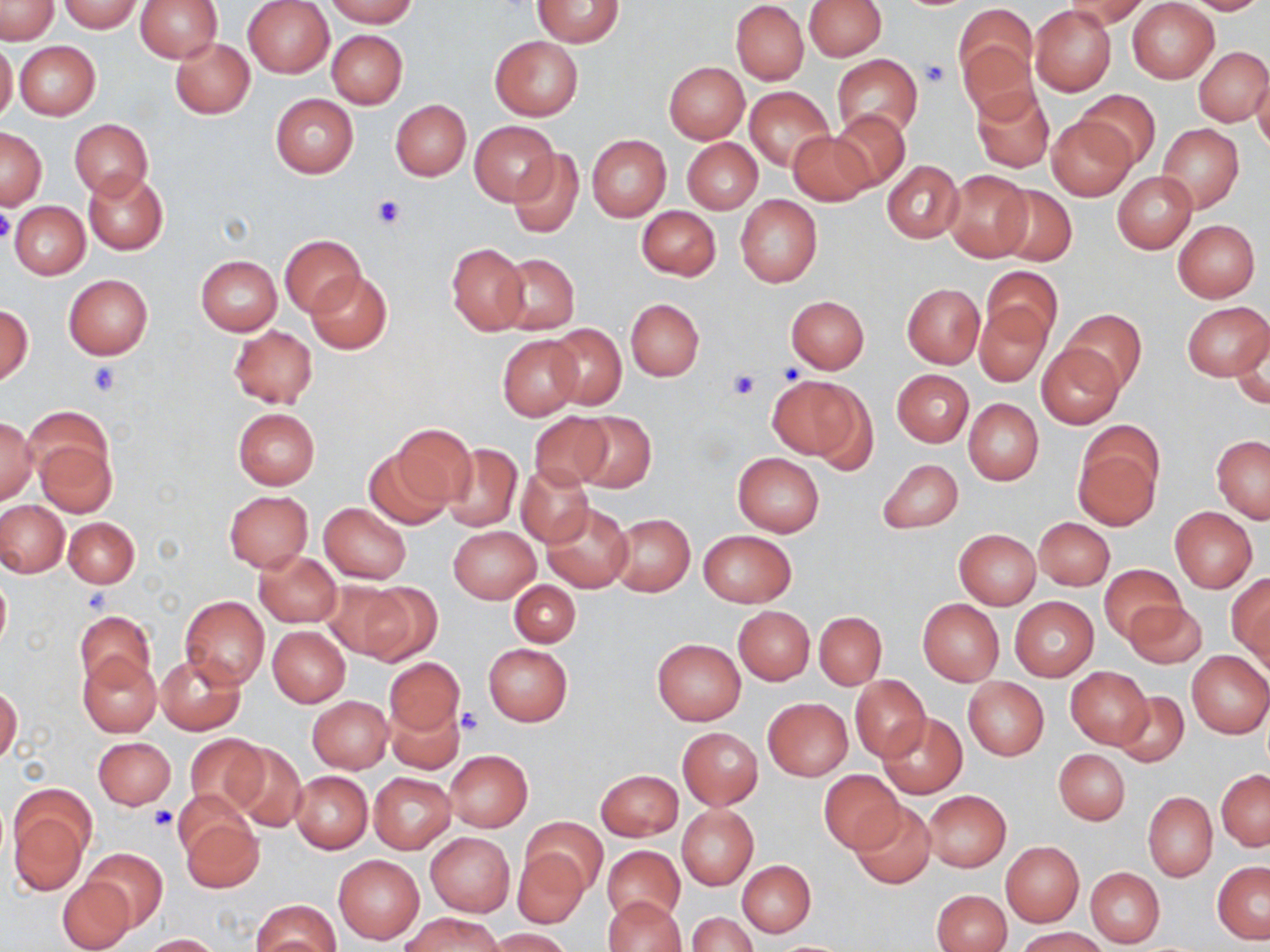 Approximate bounding boxes as named x1/y1/x2/y2 corners in pixels. Uninfected red blood cell locations: (x1=134, y1=0, x2=222, y2=62), (x1=243, y1=0, x2=333, y2=77), (x1=324, y1=0, x2=420, y2=27), (x1=533, y1=0, x2=625, y2=47), (x1=802, y1=0, x2=886, y2=60), (x1=1181, y1=0, x2=1270, y2=15), (x1=0, y1=1, x2=59, y2=43), (x1=61, y1=1, x2=143, y2=32), (x1=731, y1=1, x2=809, y2=84), (x1=1062, y1=1, x2=1147, y2=30), (x1=1127, y1=1, x2=1218, y2=84), (x1=955, y1=4, x2=1036, y2=96), (x1=1030, y1=5, x2=1116, y2=96), (x1=326, y1=29, x2=408, y2=108), (x1=491, y1=36, x2=582, y2=120), (x1=169, y1=37, x2=254, y2=120), (x1=958, y1=39, x2=1040, y2=125), (x1=0, y1=40, x2=18, y2=124), (x1=14, y1=41, x2=100, y2=120), (x1=1195, y1=46, x2=1269, y2=126), (x1=832, y1=54, x2=923, y2=138), (x1=663, y1=61, x2=749, y2=143), (x1=1251, y1=72, x2=1270, y2=153), (x1=972, y1=85, x2=1053, y2=171), (x1=745, y1=86, x2=834, y2=172), (x1=1075, y1=90, x2=1160, y2=172), (x1=271, y1=94, x2=358, y2=178), (x1=391, y1=99, x2=471, y2=181), (x1=830, y1=110, x2=910, y2=191), (x1=1047, y1=115, x2=1135, y2=200), (x1=70, y1=119, x2=152, y2=198), (x1=470, y1=121, x2=556, y2=203), (x1=1157, y1=124, x2=1244, y2=212), (x1=0, y1=128, x2=46, y2=208), (x1=787, y1=131, x2=872, y2=204), (x1=587, y1=135, x2=670, y2=220), (x1=682, y1=138, x2=761, y2=214), (x1=508, y1=147, x2=582, y2=239), (x1=883, y1=161, x2=963, y2=242), (x1=942, y1=169, x2=1033, y2=261), (x1=83, y1=171, x2=168, y2=255), (x1=1113, y1=171, x2=1196, y2=253), (x1=993, y1=183, x2=1077, y2=265), (x1=735, y1=195, x2=822, y2=287), (x1=10, y1=202, x2=89, y2=279), (x1=637, y1=206, x2=721, y2=280), (x1=1173, y1=219, x2=1260, y2=302), (x1=279, y1=234, x2=365, y2=316), (x1=446, y1=242, x2=529, y2=335), (x1=496, y1=253, x2=580, y2=335), (x1=196, y1=255, x2=283, y2=336), (x1=981, y1=266, x2=1061, y2=344), (x1=305, y1=271, x2=392, y2=355), (x1=63, y1=275, x2=153, y2=358), (x1=901, y1=283, x2=985, y2=368), (x1=786, y1=295, x2=868, y2=373), (x1=626, y1=299, x2=703, y2=380), (x1=974, y1=301, x2=1052, y2=387), (x1=1182, y1=301, x2=1269, y2=382), (x1=1, y1=304, x2=33, y2=386), (x1=1062, y1=309, x2=1146, y2=392), (x1=546, y1=323, x2=626, y2=410), (x1=229, y1=325, x2=317, y2=408), (x1=1231, y1=329, x2=1270, y2=408), (x1=497, y1=335, x2=582, y2=421), (x1=1036, y1=342, x2=1124, y2=429), (x1=892, y1=369, x2=973, y2=446), (x1=767, y1=373, x2=870, y2=464), (x1=964, y1=398, x2=1044, y2=485), (x1=26, y1=407, x2=114, y2=490), (x1=232, y1=408, x2=320, y2=488), (x1=572, y1=410, x2=657, y2=493), (x1=530, y1=412, x2=612, y2=489), (x1=0, y1=418, x2=37, y2=504), (x1=391, y1=424, x2=476, y2=510), (x1=1212, y1=435, x2=1269, y2=522), (x1=33, y1=436, x2=117, y2=518), (x1=1072, y1=438, x2=1161, y2=531), (x1=441, y1=442, x2=523, y2=532), (x1=363, y1=449, x2=452, y2=530), (x1=733, y1=452, x2=824, y2=536), (x1=877, y1=459, x2=963, y2=534), (x1=517, y1=466, x2=593, y2=546), (x1=223, y1=491, x2=312, y2=572), (x1=1, y1=500, x2=68, y2=576), (x1=543, y1=501, x2=633, y2=592), (x1=319, y1=503, x2=411, y2=583), (x1=1169, y1=506, x2=1258, y2=593), (x1=609, y1=513, x2=695, y2=597), (x1=64, y1=517, x2=139, y2=588), (x1=1034, y1=517, x2=1114, y2=590), (x1=449, y1=526, x2=539, y2=603), (x1=698, y1=529, x2=796, y2=607), (x1=954, y1=529, x2=1041, y2=608), (x1=255, y1=551, x2=342, y2=628), (x1=1099, y1=564, x2=1187, y2=643), (x1=0, y1=574, x2=11, y2=656), (x1=1228, y1=574, x2=1270, y2=663), (x1=321, y1=580, x2=413, y2=660), (x1=358, y1=580, x2=442, y2=665), (x1=509, y1=581, x2=580, y2=647), (x1=180, y1=596, x2=269, y2=689), (x1=1009, y1=596, x2=1098, y2=682), (x1=1124, y1=597, x2=1206, y2=669), (x1=917, y1=599, x2=1004, y2=685), (x1=734, y1=606, x2=814, y2=685), (x1=75, y1=611, x2=155, y2=688), (x1=815, y1=611, x2=886, y2=690), (x1=268, y1=626, x2=350, y2=706), (x1=653, y1=638, x2=745, y2=724), (x1=483, y1=643, x2=572, y2=727), (x1=1187, y1=651, x2=1270, y2=738), (x1=78, y1=652, x2=160, y2=737), (x1=157, y1=653, x2=245, y2=735), (x1=385, y1=657, x2=463, y2=735), (x1=1066, y1=667, x2=1153, y2=749), (x1=851, y1=675, x2=929, y2=762), (x1=963, y1=677, x2=1048, y2=759), (x1=0, y1=686, x2=22, y2=765), (x1=1114, y1=690, x2=1189, y2=767), (x1=308, y1=695, x2=392, y2=773), (x1=762, y1=698, x2=853, y2=781), (x1=386, y1=701, x2=465, y2=774), (x1=877, y1=713, x2=968, y2=800), (x1=677, y1=727, x2=763, y2=809), (x1=185, y1=735, x2=265, y2=812), (x1=92, y1=737, x2=175, y2=810), (x1=224, y1=743, x2=308, y2=832), (x1=1054, y1=749, x2=1129, y2=824), (x1=444, y1=751, x2=532, y2=831), (x1=596, y1=769, x2=682, y2=841), (x1=819, y1=769, x2=902, y2=855), (x1=1218, y1=770, x2=1270, y2=850), (x1=290, y1=771, x2=372, y2=853), (x1=369, y1=774, x2=454, y2=852), (x1=922, y1=789, x2=1010, y2=872), (x1=173, y1=790, x2=255, y2=862), (x1=1143, y1=791, x2=1217, y2=881), (x1=848, y1=801, x2=935, y2=889), (x1=676, y1=804, x2=758, y2=889), (x1=8, y1=806, x2=88, y2=896), (x1=179, y1=815, x2=263, y2=894), (x1=521, y1=817, x2=608, y2=895), (x1=427, y1=833, x2=514, y2=916), (x1=1001, y1=843, x2=1083, y2=926), (x1=602, y1=845, x2=684, y2=925), (x1=513, y1=847, x2=588, y2=928), (x1=86, y1=848, x2=167, y2=929), (x1=333, y1=854, x2=425, y2=945), (x1=737, y1=860, x2=815, y2=937), (x1=1212, y1=861, x2=1270, y2=943), (x1=1085, y1=867, x2=1164, y2=947), (x1=59, y1=876, x2=134, y2=951), (x1=933, y1=890, x2=1011, y2=952), (x1=603, y1=896, x2=685, y2=952), (x1=251, y1=899, x2=339, y2=951), (x1=400, y1=912, x2=505, y2=952), (x1=688, y1=912, x2=757, y2=952), (x1=1016, y1=927, x2=1107, y2=951), (x1=487, y1=928, x2=574, y2=952), (x1=144, y1=933, x2=220, y2=952). Platelet locations: (x1=921, y1=59, x2=950, y2=87), (x1=373, y1=195, x2=408, y2=228), (x1=0, y1=207, x2=15, y2=243), (x1=88, y1=361, x2=122, y2=396), (x1=775, y1=363, x2=806, y2=386), (x1=725, y1=368, x2=762, y2=399), (x1=82, y1=589, x2=112, y2=615), (x1=457, y1=708, x2=484, y2=735), (x1=147, y1=806, x2=176, y2=831). Slide-level diagnosis: no evidence of blood parasites. Thin blood film. Light microscopy. Image is 1270×952 pixels. One field of a larger specimen. May-Grünwald-Giemsa-stained preparation. 1000x magnification.